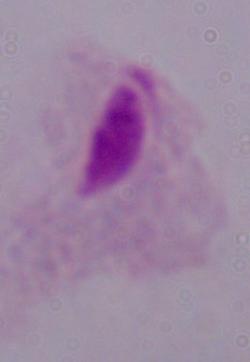 Photomicrograph. 1000x magnification. A trichomonad is shown.